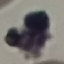
{
  "result": "negative for malaria parasites",
  "image_type": "cell patch, automatically extracted from a larger field of view and resized to 64 × 64 pixels",
  "stain": "Giemsa",
  "preparation": "thin blood smear",
  "capture": "smartphone through the microscope eyepiece"
}